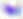
identification: Toxoplasma gondii
modality: micrograph
magnification: 400x